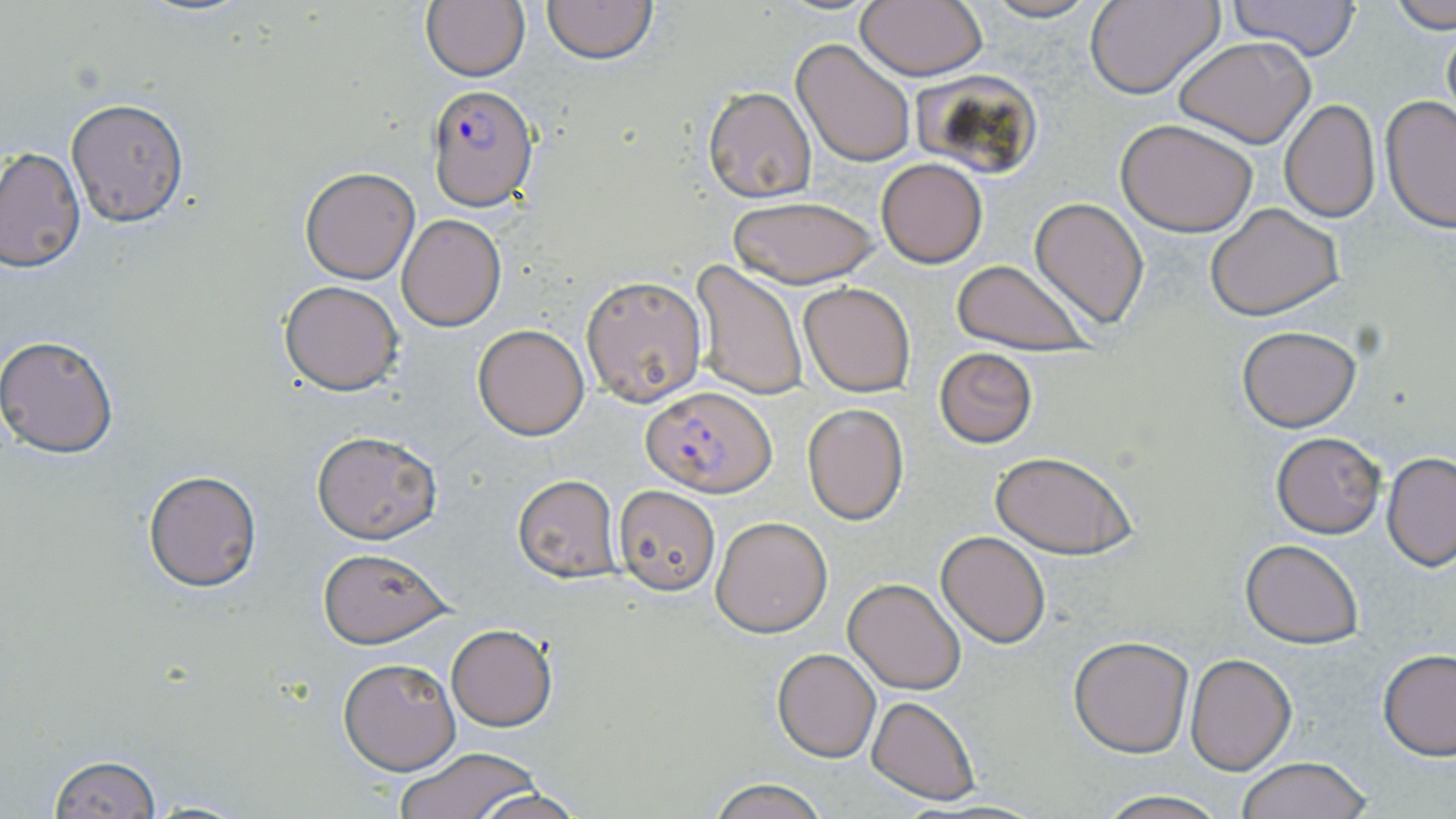
Summary:
  - Coordinate format: approximate bounding boxes as [x1, y1, x2, y2] in pixels
  - Plasmodium falciparum-infected red blood cell locations: [427, 86, 538, 209], [643, 384, 776, 496]
  - Uninfected red blood cell locations: [539, 0, 661, 64], [976, 0, 1107, 23], [1084, 0, 1224, 99], [1226, 0, 1363, 59], [422, 1, 530, 82], [855, 1, 987, 80], [1388, 2, 1455, 31], [1440, 11, 1456, 136], [1173, 37, 1317, 148], [792, 38, 917, 167], [1234, 71, 1369, 194], [702, 86, 816, 203], [1380, 95, 1456, 231], [65, 98, 191, 227], [1279, 99, 1381, 223], [1115, 118, 1259, 238], [1, 146, 84, 274], [877, 157, 987, 267], [299, 167, 420, 284], [726, 195, 879, 289], [1030, 198, 1149, 327], [1206, 204, 1344, 320], [397, 215, 506, 330], [949, 259, 1096, 358], [691, 260, 808, 400], [581, 274, 707, 406], [279, 280, 403, 394], [800, 283, 915, 395], [473, 324, 590, 439], [1236, 325, 1361, 432], [0, 334, 119, 459], [934, 348, 1038, 448], [802, 403, 909, 526], [311, 430, 442, 544], [1271, 432, 1384, 537], [991, 451, 1137, 559], [1382, 454, 1456, 570], [143, 469, 264, 592], [511, 475, 623, 583], [613, 486, 720, 594], [711, 516, 832, 637], [935, 531, 1051, 647], [1240, 539, 1364, 648], [318, 547, 453, 648], [843, 577, 966, 694], [446, 625, 558, 731], [1068, 637, 1194, 756], [772, 648, 882, 763], [1378, 650, 1456, 760], [1186, 652, 1297, 774], [338, 656, 461, 775], [867, 696, 980, 804], [394, 746, 547, 819], [47, 755, 163, 819], [1236, 757, 1374, 818], [707, 778, 833, 819], [471, 787, 587, 819], [1092, 791, 1232, 819]
  - Slide-level diagnosis: Plasmodium falciparum
  - Image size: 1456×819 pixels
  - Modality: optical microscopy
  - Field of view: single
  - Stain: May-Grünwald-Giemsa
  - Preparation: thin blood film
  - Magnification: 1000x